Outline each uninfected red blood cell.
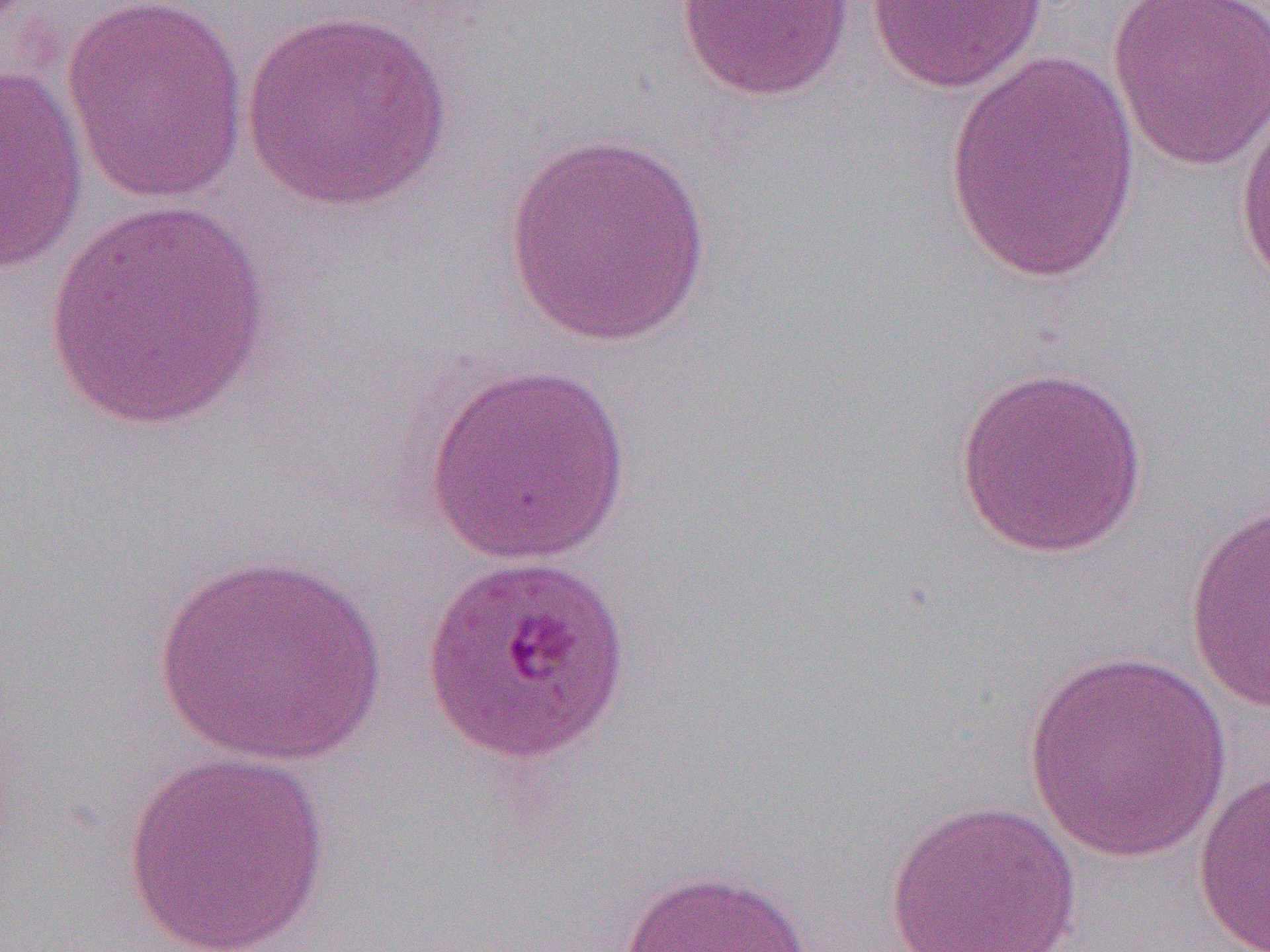

Approximate bounding boxes as (x1, y1, x2, y2) in pixels.
Uninfected red blood cells: (865, 0, 1050, 94), (1105, 0, 1270, 170), (60, 1, 250, 204), (673, 1, 858, 101), (240, 9, 453, 211), (942, 49, 1142, 285), (0, 62, 88, 274), (1234, 95, 1270, 289), (502, 130, 717, 348), (45, 195, 271, 435), (955, 363, 1151, 558), (422, 364, 633, 567), (1184, 501, 1270, 715), (153, 551, 385, 768), (1022, 651, 1234, 864), (121, 750, 334, 952), (1191, 769, 1270, 951), (884, 800, 1082, 952), (618, 867, 812, 952).

Summary:
  - Slide-level diagnosis: Plasmodium falciparum
  - Magnification: 1000x
  - Preparation: thin blood film
  - Modality: light microscopy
  - Field of view: one of a larger specimen
  - Image size: 1270×952 pixels